Name the parasite shown.
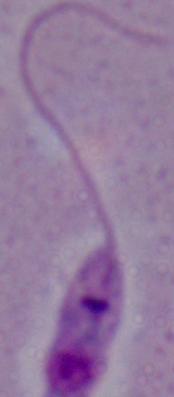

Leishmania.

1000x magnification. Micrograph.